Report the malaria status of this cell.
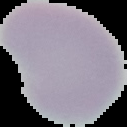
Uninfected.

Summary:
  - Preparation: thin blood film
  - Image type: segmented cell region with the area outside set to black
  - Image size: 127×127 pixels